Assess the morphology of the erythrocytes.
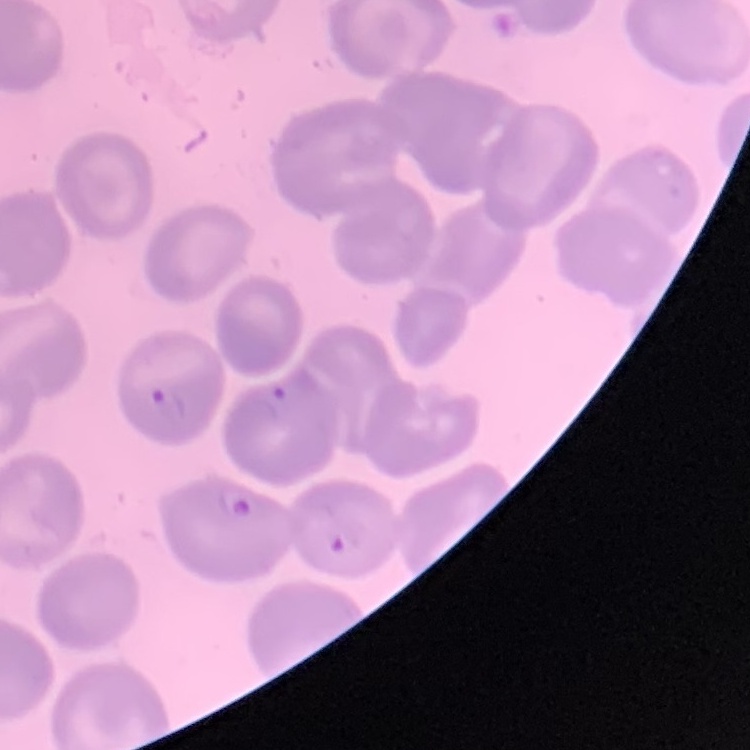
They show no rouleaux formation.

{
  "stain": "Field's or Giemsa",
  "image_type": "one tile cut from a larger photomicrograph",
  "preparation": "thin blood film"
}